Give the position of every leukocyte visible.
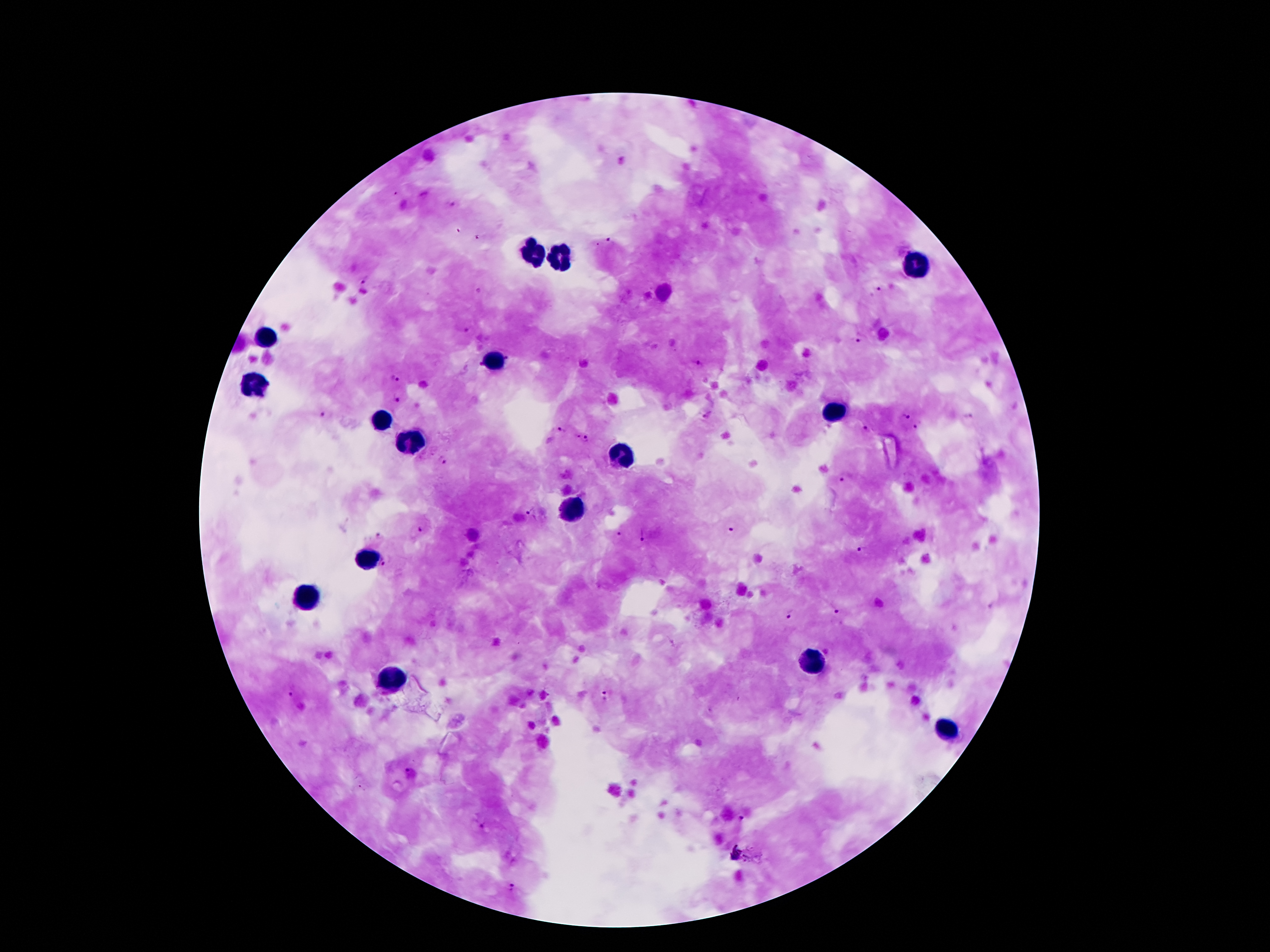

Approximate object centers, in pixels from the top-left corner.
Leukocytes: (x=534, y=250), (x=560, y=257), (x=914, y=265), (x=266, y=339), (x=494, y=360), (x=255, y=385), (x=837, y=413), (x=381, y=420), (x=407, y=440), (x=622, y=454), (x=575, y=510), (x=366, y=556), (x=307, y=600), (x=812, y=660), (x=387, y=679), (x=945, y=733).

malaria parasite locations = (x=608, y=242), (x=366, y=279), (x=877, y=289), (x=466, y=328), (x=858, y=337), (x=694, y=361), (x=394, y=377), (x=398, y=397), (x=325, y=414), (x=707, y=414), (x=904, y=417), (x=967, y=417), (x=917, y=426), (x=560, y=429), (x=867, y=431), (x=586, y=438), (x=444, y=459), (x=842, y=478), (x=531, y=511), (x=730, y=528), (x=421, y=530), (x=618, y=533), (x=643, y=533), (x=379, y=536), (x=861, y=548), (x=384, y=561), (x=837, y=610), (x=790, y=614), (x=295, y=692), (x=605, y=696), (x=410, y=770), (x=740, y=818), (x=484, y=825), (x=515, y=889)
capture = smartphone through the microscope eyepiece
field of view = single
magnification = 100x
stain = Giemsa
patient malaria status = infected with Plasmodium falciparum
image size = 1270×952 pixels
preparation = thick peripheral-blood smear